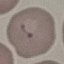
Result: malaria parasites detected. Photographed with a smartphone camera at the microscope eyepiece. Cell patch, automatically extracted from a larger field of view and resized to 64 × 64 pixels. Giemsa stain. Thin blood smear.